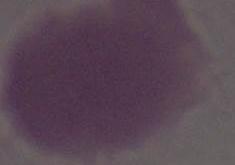

modality: micrograph
identification: erythrocyte
magnification: 1000x